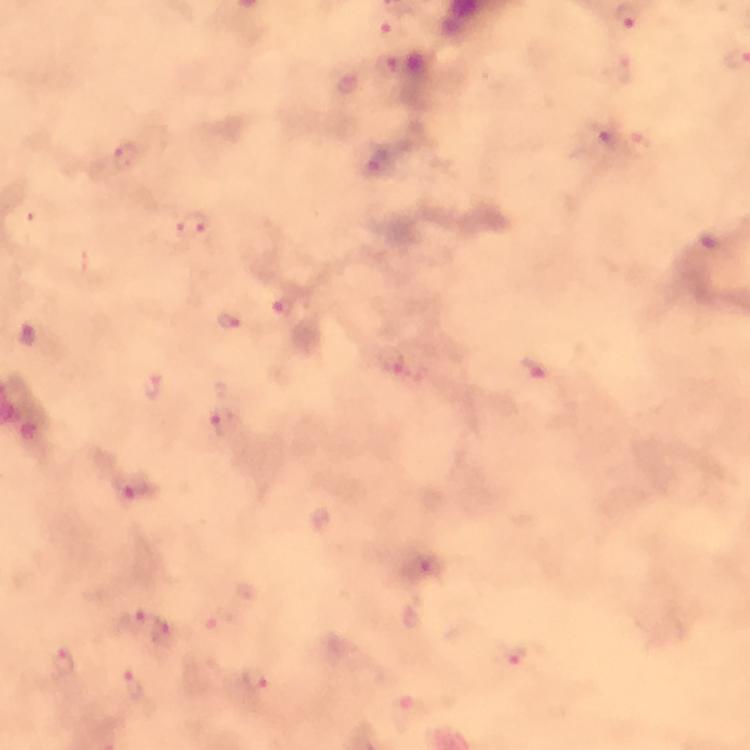
Approximate object centers, in pixels from the top-left corner. Malaria parasite locations: (x=396, y=29), (x=348, y=84), (x=606, y=134), (x=637, y=143), (x=124, y=154), (x=190, y=224), (x=282, y=307), (x=229, y=322), (x=535, y=373), (x=151, y=385), (x=226, y=425), (x=132, y=487), (x=132, y=619), (x=164, y=633), (x=516, y=657), (x=62, y=662), (x=254, y=681), (x=136, y=686). Image is 750×750 pixels. Giemsa-stained preparation. Cropped region of a single field of view. Immersion oil applied. From a diagnostic examination for malaria. At 100x magnification. Thick blood film. Photographed with a smartphone mounted on the microscope.